State which parasite is depicted.
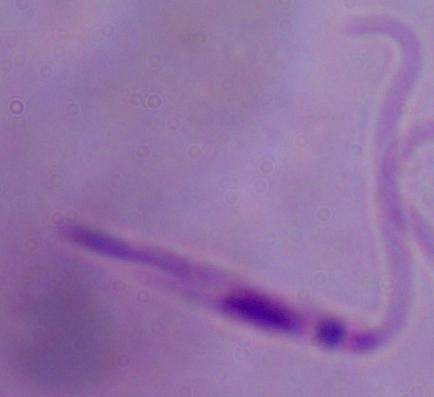
This is Leishmania.

modality = photomicrograph
magnification = 1000x